Assess this cell for malaria.
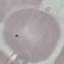

It is uninfected.

preparation = thin blood film
image type = cell patch, automatically extracted from a larger field of view and resized to 64 × 64 pixels
capture = smartphone through the microscope eyepiece
stain = Giemsa